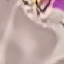

result = negative for malaria parasites
image type = automatically extracted cell patch, resized to 64 × 64 pixels
stain = Giemsa
capture = smartphone through the microscope eyepiece
preparation = thin blood smear